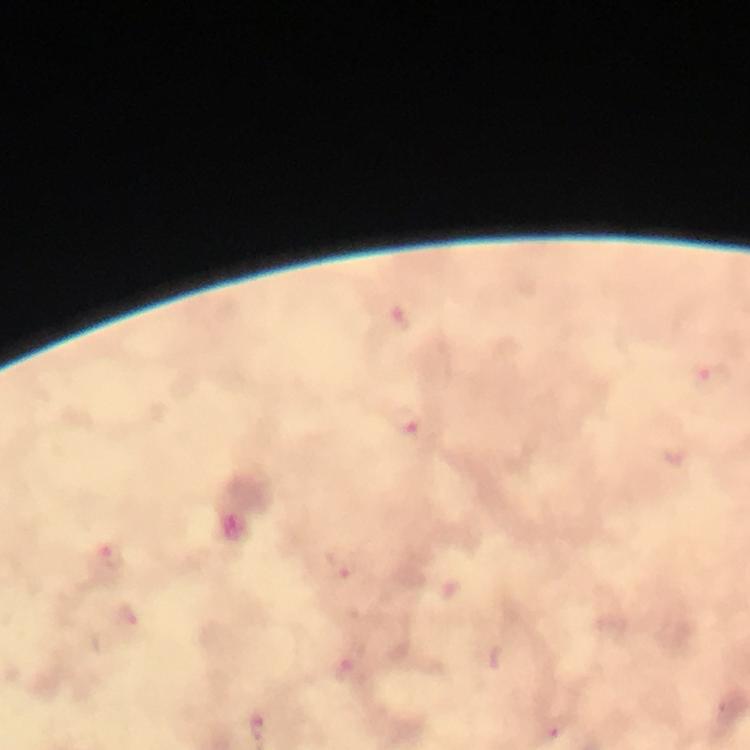
Approximate object centers, in pixels from the top-left corner. Plasmodium parasite locations: (x=713, y=378), (x=408, y=422), (x=112, y=557), (x=342, y=565), (x=555, y=729). 100x magnification. A crop from one field of view. Smartphone photograph taken through a microscope. From a diagnostic examination for malaria. Thick blood film. Giemsa stain. Image is 750×750 pixels. Immersion oil applied.